Report the malaria status of this cell.
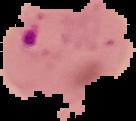

It is parasitized.

image size = 136×121 pixels
image type = cell region segmented out of the field of view; surrounding area masked to black
preparation = thin blood film